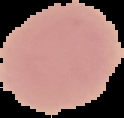

image type = cell region segmented out of the field of view; surrounding area masked to black
image size = 124×118 pixels
preparation = thin blood smear
malaria status = uninfected